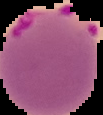 Image is 103×115 pixels. From a thin blood smear. Result: malaria parasites detected. Cell region segmented out of the field of view; the surrounding area is masked to black.